Classify this cell by malaria status.
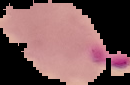
Parasitized.

preparation = thin blood film
image size = 130×85 pixels
image type = cell region segmented out of the field of view; surrounding area masked to black